State which parasite is depicted.
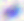
Toxoplasma gondii.

Micrograph. Captured at 400x magnification.